Identify the blood parasite species.
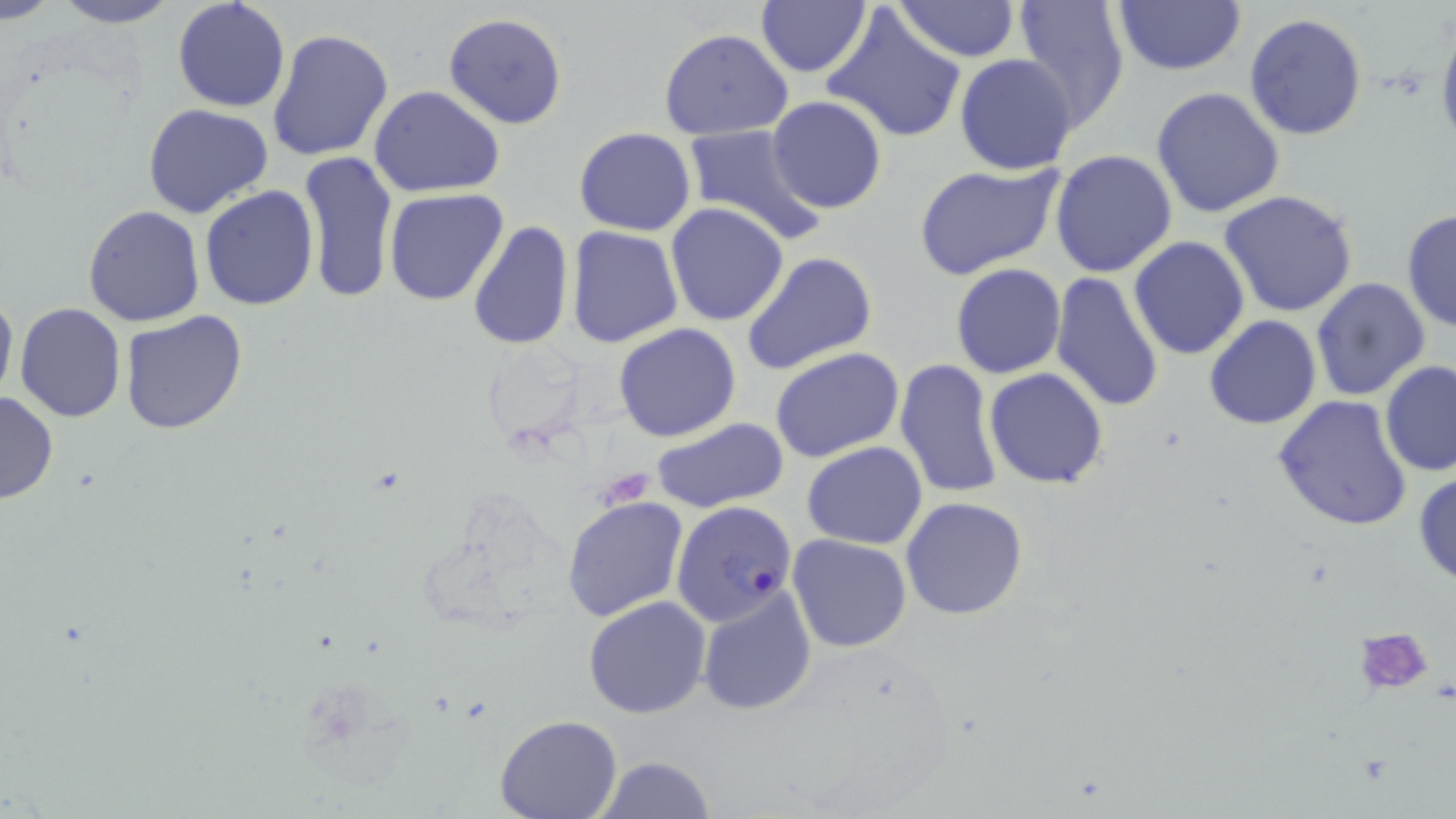

Plasmodium falciparum.

Summary:
  - Coordinate format: approximate bounding boxes as [x1, y1, x2, y2] in pixels
  - Platelet locations: [1352, 626, 1438, 698]
  - Plasmodium falciparum-infected red blood cell locations: [671, 502, 799, 625]
  - Uninfected red blood cell locations: [1, 0, 61, 23], [50, 0, 182, 28], [172, 0, 290, 112], [755, 0, 872, 79], [892, 0, 1021, 64], [1013, 0, 1132, 134], [1113, 0, 1244, 75], [822, 5, 968, 146], [442, 13, 569, 130], [1243, 13, 1368, 140], [267, 27, 395, 162], [659, 29, 795, 140], [953, 54, 1078, 176], [370, 86, 507, 198], [1150, 86, 1285, 217], [766, 96, 887, 214], [143, 103, 274, 219], [679, 124, 828, 248], [574, 127, 696, 236], [1050, 149, 1179, 279], [299, 150, 396, 305], [913, 162, 1065, 282], [200, 186, 318, 311], [384, 189, 509, 307], [1219, 191, 1359, 318], [664, 202, 790, 327], [83, 204, 206, 328], [1402, 209, 1456, 337], [467, 220, 574, 353], [567, 227, 682, 348], [1129, 235, 1249, 359], [741, 251, 878, 376], [951, 263, 1068, 379], [1049, 272, 1164, 414], [1309, 277, 1431, 401], [0, 285, 17, 407], [14, 302, 125, 422], [118, 309, 247, 437], [1203, 314, 1323, 430], [613, 323, 743, 442], [770, 347, 904, 463], [894, 357, 1005, 501], [1380, 362, 1456, 478], [985, 368, 1109, 488], [0, 390, 58, 505], [1272, 395, 1415, 531], [651, 416, 790, 513], [802, 442, 928, 548], [1413, 470, 1456, 587], [562, 496, 690, 622], [901, 496, 1031, 620], [786, 534, 913, 654], [698, 585, 817, 715], [582, 596, 710, 718], [495, 715, 620, 819], [594, 756, 717, 819]
  - Stain: May-Grünwald-Giemsa
  - Field of view: single
  - Preparation: thin blood smear
  - Magnification: 1000x
  - Image size: 1456×819 pixels
  - Modality: light microscopy